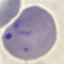
Summary:
  - Malaria status: parasitized
  - Image type: cell patch, automatically extracted from a larger field of view and resized to 64 × 64 pixels
  - Stain: Giemsa
  - Capture: smartphone through the microscope eyepiece
  - Preparation: thin blood smear